Name the parasite shown.
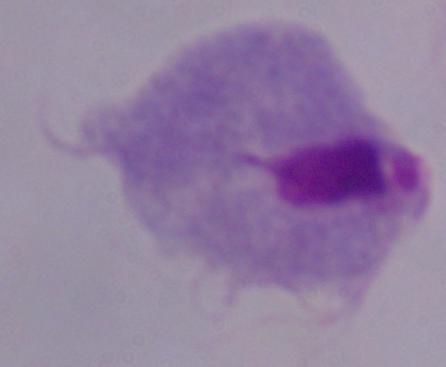
A trichomonad.

Captured at 1000x magnification. Photomicrograph.